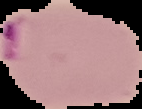

{
  "image_type": "segmented cell region on a black background",
  "preparation": "thin blood smear",
  "image_size": "142×109 pixels",
  "malaria_status": "parasitized"
}